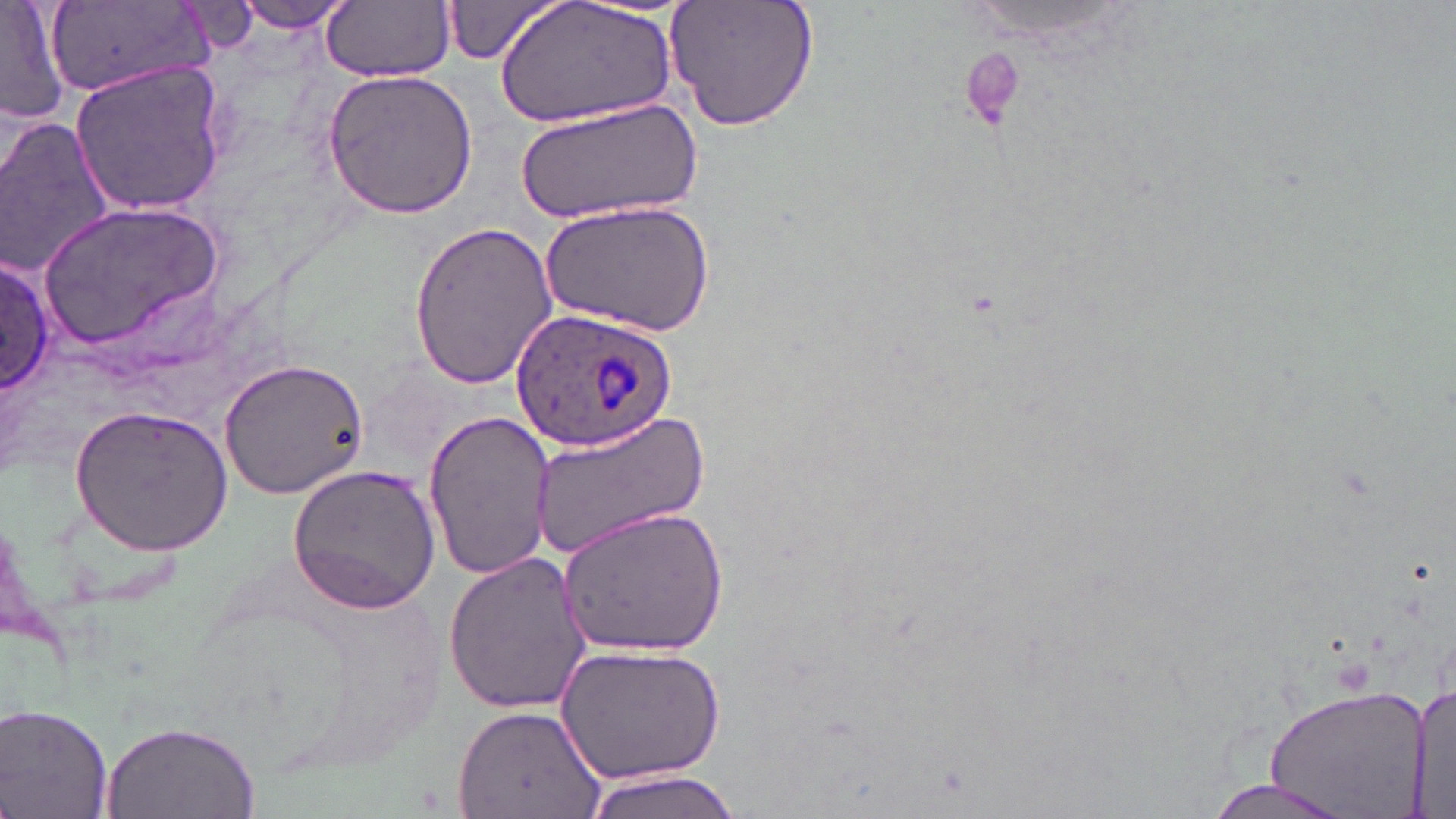 Approximate bounding boxes as [x1, y1, x2, y2] in pixels. Uninfected red blood cell locations: [0, 0, 70, 126], [230, 0, 361, 33], [665, 0, 819, 132], [322, 1, 455, 82], [437, 1, 566, 66], [500, 1, 676, 127], [47, 2, 212, 98], [70, 59, 229, 215], [322, 69, 479, 219], [519, 96, 702, 223], [0, 117, 120, 278], [541, 201, 715, 338], [42, 207, 224, 346], [407, 220, 559, 388], [1, 252, 56, 397], [219, 356, 369, 499], [71, 404, 234, 553], [525, 406, 714, 560], [422, 409, 555, 580], [287, 462, 444, 616], [555, 504, 730, 658], [442, 550, 594, 716], [560, 640, 726, 784], [1413, 677, 1451, 819], [1261, 684, 1433, 814], [451, 703, 605, 819], [1, 704, 117, 819], [100, 724, 260, 819], [577, 769, 753, 819], [1201, 778, 1355, 819]. Plasmodium ovale-infected red blood cell locations: [509, 305, 679, 452]. Platelet locations: [959, 48, 1026, 131]. Slide-level diagnosis: Plasmodium ovale. Light microscopy. One field of a larger specimen. Thin blood film. Image is 1456×819 pixels. Captured at 1000x magnification. May-Grünwald-Giemsa-stained preparation.